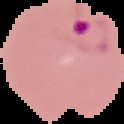
preparation = thin blood smear
malaria status = parasitized
image size = 124×124 pixels
image type = segmented cell region with the area outside set to black